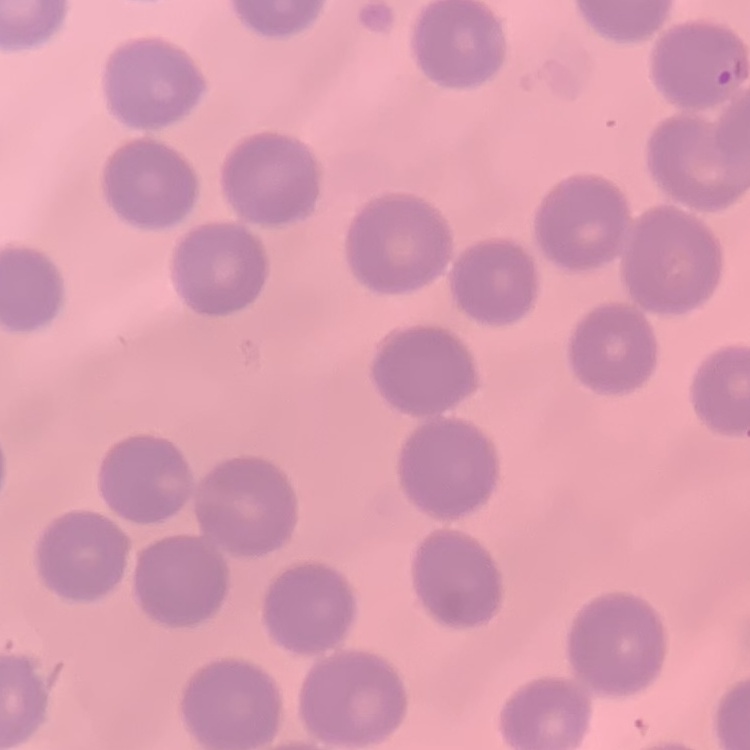

The red blood cells show no rouleaux formation. Stained with either Field's or Giemsa. Square crop of a larger photomicrograph. Thin peripheral smear.